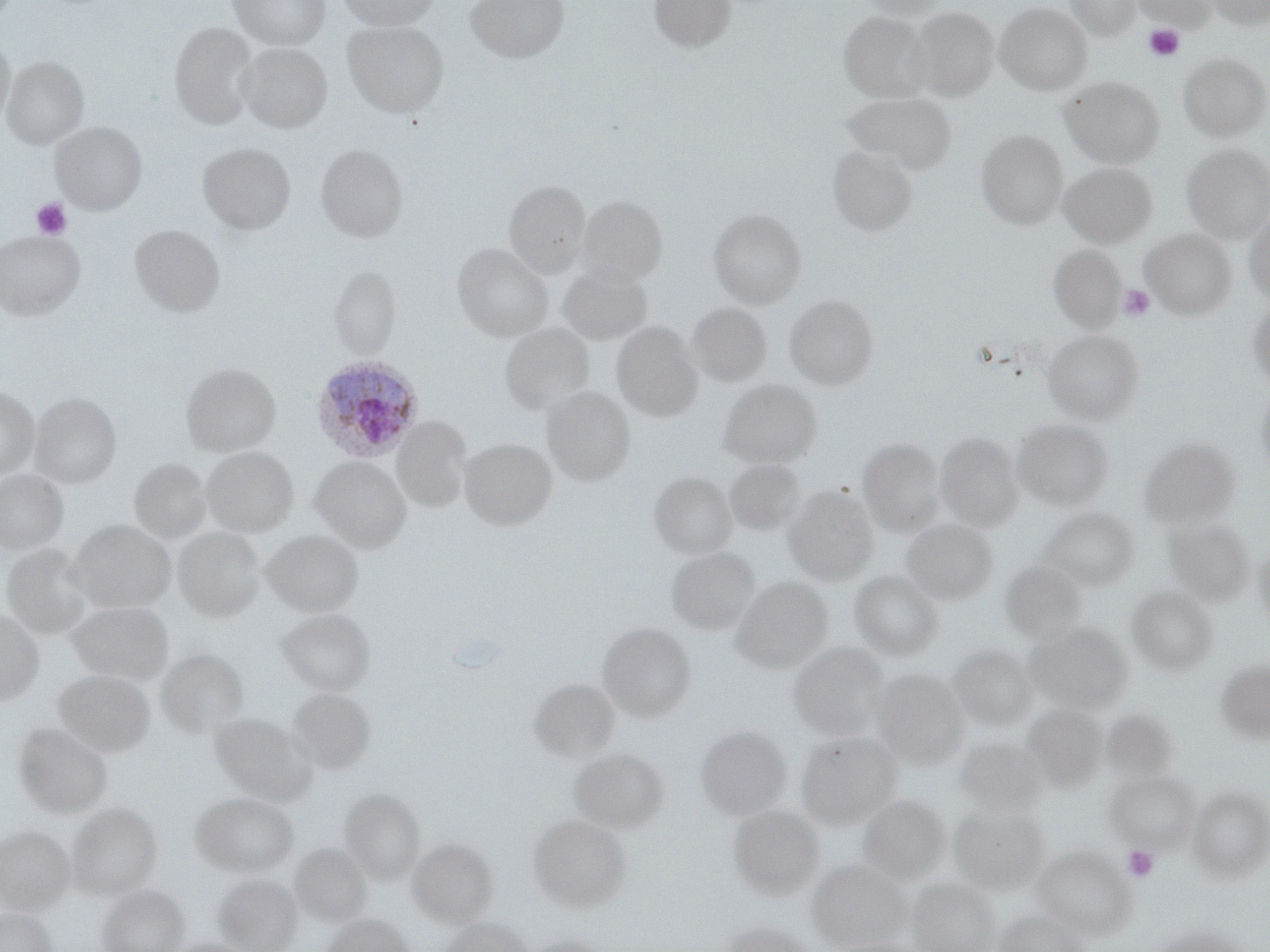
Summary:
  - Coordinate format: approximate bounding boxes as [x1, y1, x2, y2] in pixels
  - Plasmodium ovale-infected red blood cell locations: [311, 356, 424, 462]
  - Platelet locations: [1144, 24, 1185, 62], [31, 198, 72, 240], [1117, 283, 1158, 322], [1123, 846, 1159, 882]
  - Uninfected red blood cell locations: [229, 0, 330, 50], [336, 0, 440, 30], [466, 0, 569, 64], [649, 0, 736, 54], [857, 0, 949, 21], [1065, 0, 1141, 40], [1137, 0, 1213, 31], [1204, 0, 1270, 28], [995, 3, 1092, 95], [910, 7, 998, 100], [839, 11, 932, 101], [343, 19, 449, 119], [169, 23, 258, 129], [0, 38, 15, 131], [237, 43, 332, 133], [1179, 53, 1269, 140], [2, 56, 88, 149], [1061, 77, 1164, 168], [842, 92, 957, 176], [51, 122, 147, 215], [976, 130, 1068, 229], [198, 142, 296, 234], [315, 144, 407, 243], [1181, 144, 1270, 242], [828, 145, 918, 236], [1058, 162, 1156, 248], [504, 180, 590, 277], [577, 195, 667, 285], [708, 208, 806, 308], [1243, 208, 1270, 305], [130, 224, 225, 317], [1140, 229, 1236, 319], [0, 230, 85, 320], [452, 243, 552, 342], [1047, 244, 1126, 333], [559, 264, 651, 344], [328, 266, 401, 360], [784, 295, 878, 390], [1245, 296, 1270, 391], [687, 302, 770, 386], [500, 322, 593, 415], [611, 322, 703, 422], [1043, 330, 1143, 424], [181, 362, 281, 457], [718, 379, 822, 469], [1255, 382, 1270, 483], [0, 386, 39, 480], [543, 386, 635, 486], [29, 392, 121, 488], [392, 417, 471, 513], [1012, 418, 1113, 510], [935, 432, 1024, 532], [1139, 436, 1241, 529], [858, 437, 945, 535], [459, 438, 556, 530], [202, 446, 298, 537], [311, 456, 411, 553], [129, 459, 211, 543], [724, 460, 805, 537], [0, 469, 69, 556], [649, 472, 737, 559], [785, 486, 878, 585], [1038, 507, 1140, 591], [1164, 516, 1253, 605], [902, 519, 997, 604], [69, 520, 174, 613], [174, 527, 265, 622], [262, 529, 363, 618], [1252, 542, 1270, 633], [2, 543, 97, 640], [666, 547, 760, 635], [1002, 562, 1087, 645], [848, 570, 944, 662], [730, 577, 832, 674], [1127, 585, 1218, 674], [65, 601, 174, 685], [275, 608, 376, 696], [0, 609, 44, 705], [597, 622, 696, 722], [1027, 622, 1131, 713], [788, 642, 889, 740], [948, 644, 1038, 730], [156, 648, 249, 738], [1214, 657, 1270, 744], [870, 669, 969, 768], [54, 670, 155, 757], [530, 679, 618, 761], [287, 688, 375, 774], [1022, 704, 1107, 791], [210, 712, 316, 806], [14, 722, 112, 818], [695, 726, 791, 821], [796, 731, 903, 828], [955, 737, 1048, 816], [568, 748, 670, 834], [1107, 770, 1198, 851], [1188, 786, 1270, 881], [339, 788, 426, 884], [190, 792, 299, 878], [858, 794, 948, 886], [67, 802, 162, 899], [949, 802, 1049, 894], [728, 804, 824, 899], [528, 814, 631, 913], [0, 826, 75, 915], [408, 837, 498, 927], [290, 843, 371, 927], [1033, 846, 1132, 937], [809, 859, 911, 949], [213, 874, 303, 952], [907, 878, 1000, 952], [98, 884, 189, 952], [0, 907, 58, 952], [993, 910, 1088, 952], [322, 913, 414, 952], [438, 916, 533, 952], [720, 919, 816, 952], [1149, 925, 1247, 952], [516, 935, 613, 952], [166, 938, 258, 952], [825, 938, 927, 952]
  - Slide-level diagnosis: Plasmodium ovale
  - Preparation: thin blood smear
  - Modality: light microscopy
  - Image size: 1270×952 pixels
  - Field of view: one of a larger specimen
  - Stain: May-Grünwald-Giemsa
  - Magnification: 1000x